Classify this cell by malaria status.
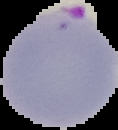
Parasitized.

preparation = thin blood film
image size = 118×130 pixels
image type = segmented cell region with the area outside set to black